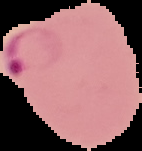
Segmented cell region on a black background. From a thin blood smear. Result: Plasmodium parasites identified. Image is 142×151 pixels.